Classify this cell by malaria status.
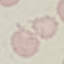

It is uninfected.

stain = Giemsa
preparation = thin smear
image type = cell patch, automatically extracted from a larger field of view and resized to 64 × 64 pixels
capture = smartphone through the microscope eyepiece